Locate every blood parasite and identify its species.
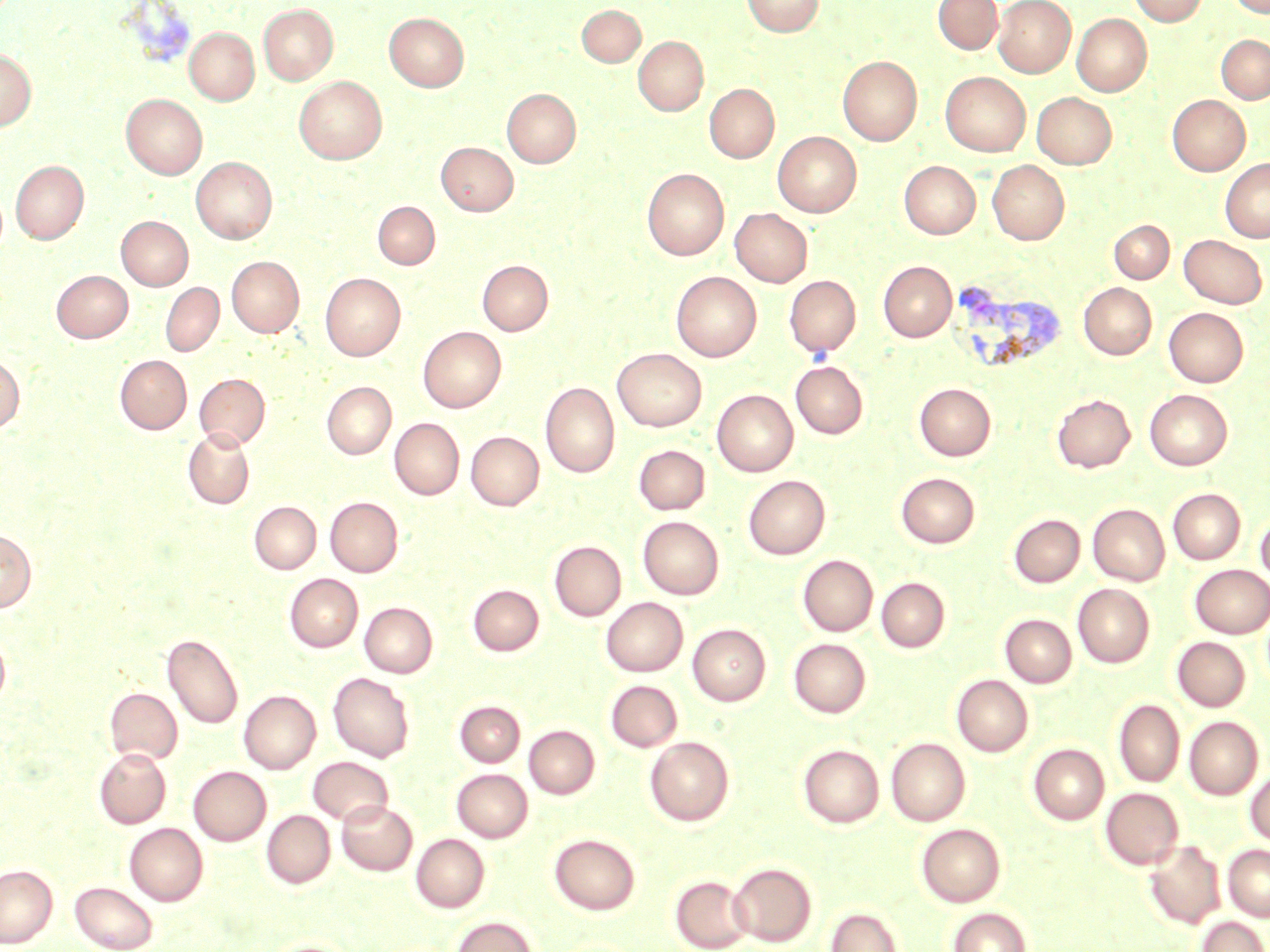

Approximate bounding boxes as named x1/y1/x2/y2 corners in pixels.
Plasmodium vivax-infected red blood cells: (x1=955, y1=283, x2=1066, y2=371).
No Plasmodium falciparum, Plasmodium ovale, Plasmodium malariae, Babesia divergens, or Trypanosoma brucei observed.

Summary:
  - Uninfected red blood cell locations: (x1=742, y1=0, x2=824, y2=37), (x1=933, y1=0, x2=1002, y2=54), (x1=994, y1=0, x2=1076, y2=76), (x1=1128, y1=0, x2=1207, y2=26), (x1=1228, y1=0, x2=1269, y2=17), (x1=259, y1=5, x2=337, y2=84), (x1=577, y1=5, x2=645, y2=66), (x1=384, y1=12, x2=469, y2=91), (x1=1072, y1=14, x2=1151, y2=96), (x1=184, y1=27, x2=259, y2=105), (x1=1216, y1=35, x2=1270, y2=103), (x1=633, y1=36, x2=708, y2=115), (x1=0, y1=48, x2=36, y2=130), (x1=838, y1=55, x2=922, y2=145), (x1=941, y1=72, x2=1030, y2=156), (x1=294, y1=77, x2=386, y2=164), (x1=705, y1=84, x2=779, y2=163), (x1=502, y1=88, x2=581, y2=167), (x1=1032, y1=92, x2=1116, y2=169), (x1=121, y1=94, x2=207, y2=179), (x1=1168, y1=95, x2=1250, y2=175), (x1=773, y1=131, x2=861, y2=216), (x1=436, y1=142, x2=518, y2=215), (x1=191, y1=157, x2=277, y2=243), (x1=1220, y1=158, x2=1270, y2=242), (x1=11, y1=160, x2=88, y2=243), (x1=988, y1=160, x2=1069, y2=245), (x1=900, y1=161, x2=980, y2=238), (x1=643, y1=168, x2=729, y2=259), (x1=373, y1=201, x2=440, y2=270), (x1=730, y1=208, x2=812, y2=286), (x1=116, y1=216, x2=193, y2=290), (x1=1109, y1=220, x2=1174, y2=283), (x1=1179, y1=234, x2=1267, y2=308), (x1=226, y1=256, x2=304, y2=337), (x1=478, y1=260, x2=552, y2=335), (x1=879, y1=262, x2=957, y2=341), (x1=52, y1=270, x2=133, y2=342), (x1=671, y1=272, x2=761, y2=361), (x1=321, y1=273, x2=405, y2=360), (x1=785, y1=275, x2=860, y2=357), (x1=161, y1=282, x2=224, y2=356), (x1=1079, y1=283, x2=1156, y2=359), (x1=1164, y1=308, x2=1248, y2=386), (x1=418, y1=326, x2=505, y2=412), (x1=612, y1=348, x2=706, y2=431), (x1=0, y1=355, x2=24, y2=433), (x1=116, y1=355, x2=192, y2=433), (x1=791, y1=361, x2=868, y2=438), (x1=194, y1=373, x2=270, y2=449), (x1=322, y1=382, x2=396, y2=459), (x1=541, y1=382, x2=619, y2=477), (x1=915, y1=383, x2=996, y2=460), (x1=712, y1=389, x2=798, y2=476), (x1=1145, y1=389, x2=1232, y2=470), (x1=1052, y1=394, x2=1135, y2=472), (x1=390, y1=418, x2=464, y2=499), (x1=183, y1=429, x2=255, y2=509), (x1=466, y1=431, x2=544, y2=510), (x1=634, y1=445, x2=710, y2=515), (x1=896, y1=472, x2=980, y2=548), (x1=743, y1=475, x2=829, y2=559), (x1=1168, y1=488, x2=1245, y2=564), (x1=325, y1=497, x2=403, y2=576), (x1=249, y1=501, x2=321, y2=574), (x1=1088, y1=503, x2=1170, y2=585), (x1=1256, y1=512, x2=1270, y2=584), (x1=1009, y1=514, x2=1085, y2=587), (x1=638, y1=516, x2=724, y2=599), (x1=0, y1=530, x2=36, y2=611), (x1=550, y1=541, x2=625, y2=620), (x1=798, y1=555, x2=877, y2=635), (x1=1190, y1=564, x2=1270, y2=638), (x1=285, y1=574, x2=363, y2=652), (x1=877, y1=577, x2=949, y2=651), (x1=1073, y1=583, x2=1154, y2=667), (x1=468, y1=585, x2=543, y2=656), (x1=601, y1=597, x2=687, y2=676), (x1=360, y1=602, x2=437, y2=677), (x1=1001, y1=614, x2=1076, y2=687), (x1=688, y1=623, x2=770, y2=705), (x1=0, y1=632, x2=10, y2=706), (x1=163, y1=633, x2=243, y2=729), (x1=1172, y1=637, x2=1250, y2=711), (x1=789, y1=639, x2=870, y2=717), (x1=328, y1=672, x2=414, y2=762), (x1=952, y1=674, x2=1033, y2=756), (x1=606, y1=680, x2=682, y2=751), (x1=105, y1=688, x2=182, y2=764), (x1=239, y1=690, x2=320, y2=773), (x1=1114, y1=699, x2=1185, y2=787), (x1=455, y1=700, x2=525, y2=767), (x1=1185, y1=716, x2=1263, y2=799), (x1=524, y1=725, x2=599, y2=799), (x1=645, y1=737, x2=734, y2=825), (x1=886, y1=737, x2=970, y2=826), (x1=1029, y1=743, x2=1109, y2=824), (x1=798, y1=745, x2=884, y2=827), (x1=94, y1=748, x2=170, y2=828), (x1=308, y1=756, x2=393, y2=826), (x1=189, y1=766, x2=271, y2=845), (x1=452, y1=769, x2=533, y2=841), (x1=1246, y1=771, x2=1270, y2=846), (x1=1101, y1=787, x2=1183, y2=869), (x1=337, y1=801, x2=417, y2=875), (x1=262, y1=810, x2=335, y2=888), (x1=124, y1=823, x2=208, y2=905), (x1=917, y1=823, x2=1005, y2=906), (x1=411, y1=833, x2=489, y2=912), (x1=549, y1=833, x2=640, y2=914), (x1=1144, y1=840, x2=1225, y2=928), (x1=1224, y1=844, x2=1270, y2=921), (x1=728, y1=863, x2=816, y2=946), (x1=0, y1=864, x2=57, y2=947), (x1=670, y1=875, x2=752, y2=951), (x1=70, y1=882, x2=157, y2=952), (x1=827, y1=907, x2=902, y2=952), (x1=948, y1=907, x2=1031, y2=952), (x1=451, y1=916, x2=538, y2=952), (x1=1198, y1=916, x2=1268, y2=952), (x1=263, y1=940, x2=357, y2=952)
  - Slide-level diagnosis: Plasmodium vivax
  - Magnification: 1000x
  - Field of view: single
  - Image size: 1270×952 pixels
  - Stain: May-Grünwald-Giemsa
  - Modality: light microscopy
  - Preparation: thin blood smear